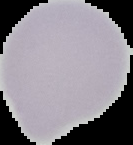

Image is 133×145 pixels. Malaria status: uninfected. Cell region segmented out of the field of view; the surrounding area is masked to black. From a thin blood film.